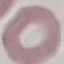
Result: no malaria parasites seen. Photographed with a smartphone camera at the microscope eyepiece. Thin blood film. Giemsa-stained preparation. Automatically extracted cell patch, resized to 64 × 64 pixels.